Give the extent of all Plasmodium ovale-infected red blood cells.
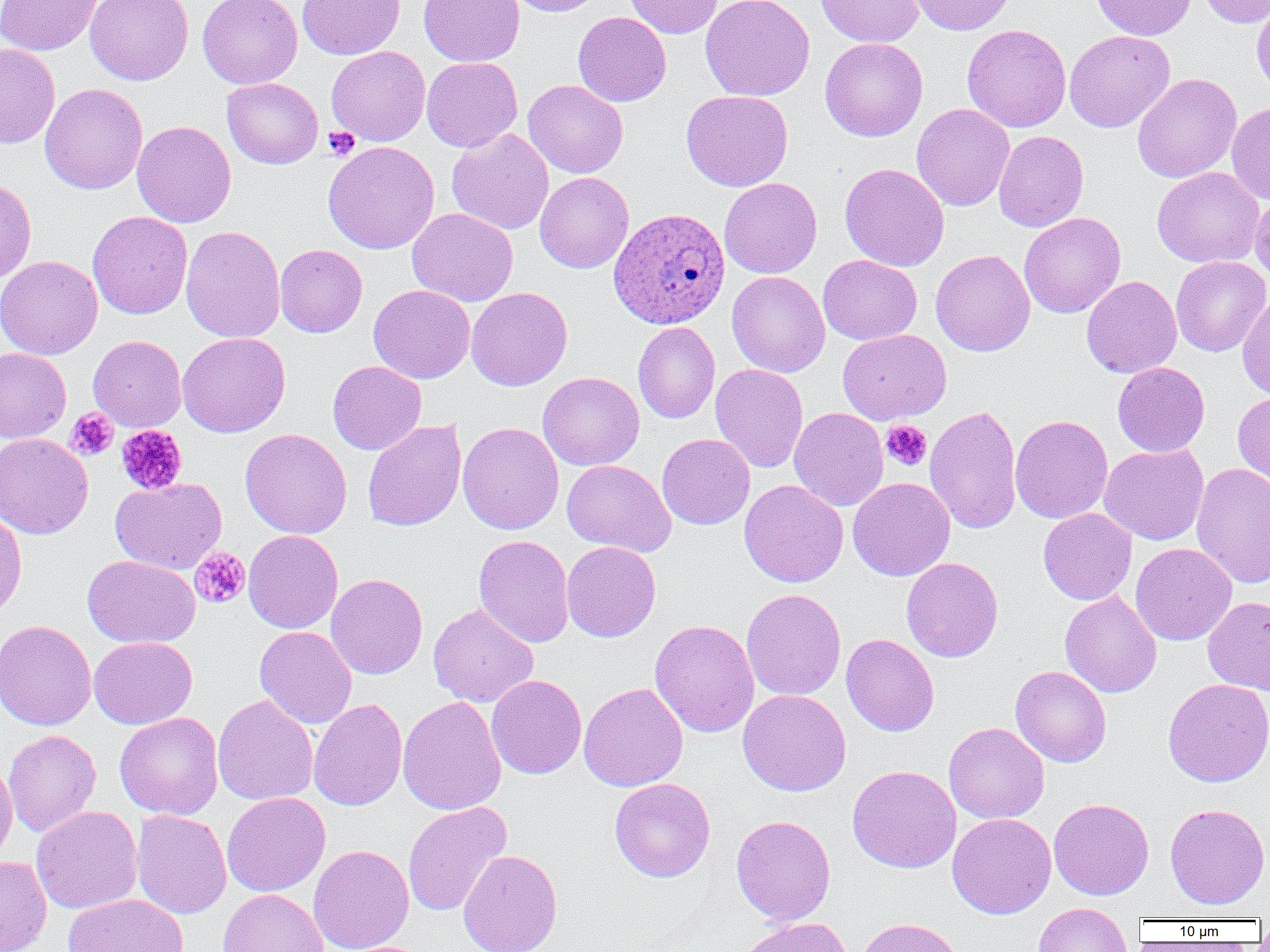

Approximate bounding boxes as (x1,y1)-(x2,y2) corner pairs in pixels.
Plasmodium ovale-infected red blood cells: (609,207)-(730,329).

{
  "slide_level_diagnosis": "Plasmodium ovale",
  "image_size": "1270×952 pixels",
  "magnification": "1000x",
  "preparation": "thin blood smear",
  "field_of_view": "one of a larger specimen",
  "modality": "light microscopy",
  "platelet_locations": "approximate bounding boxes as (x1,y1)-(x2,y2) corner pairs in pixels: (322,126)-(360,160), (64,407)-(119,461), (881,420)-(932,471), (116,424)-(188,495), (189,547)-(251,609)",
  "uninfected_red_blood_cell_locations": "approximate bounding boxes as (x1,y1)-(x2,y2) corner pairs in pixels: (0,0)-(102,55), (85,0)-(194,86), (197,0)-(303,89), (297,0)-(404,60), (419,0)-(524,67), (505,0)-(608,16), (623,0)-(723,38), (700,0)-(815,101), (815,0)-(924,47), (907,0)-(1015,35), (1091,0)-(1196,41), (1197,0)-(1270,28), (1251,2)-(1270,97), (573,11)-(672,107), (962,24)-(1071,132), (1064,30)-(1175,133), (820,37)-(928,141), (0,43)-(60,149), (326,46)-(430,146), (421,57)-(522,152), (1132,73)-(1242,183), (222,78)-(323,169), (522,79)-(628,178), (40,83)-(147,194), (681,90)-(793,191), (1227,101)-(1270,204), (911,104)-(1014,211), (132,120)-(236,228), (447,128)-(554,235), (993,130)-(1089,232), (322,141)-(439,254), (839,162)-(950,271), (1152,167)-(1264,268), (535,172)-(634,273), (0,176)-(37,283), (719,177)-(822,278), (1249,193)-(1270,283), (407,208)-(518,307), (87,211)-(192,319), (1019,212)-(1126,318), (181,225)-(285,343), (275,244)-(367,337), (930,249)-(1035,356), (818,254)-(922,345), (0,255)-(102,359), (1170,256)-(1269,356), (727,271)-(830,377), (1081,275)-(1182,378), (369,284)-(475,383), (466,287)-(572,391), (1237,292)-(1270,402), (633,322)-(720,424), (837,329)-(951,424), (178,332)-(290,437), (88,335)-(186,432), (0,347)-(71,443), (327,360)-(426,455), (1113,362)-(1210,457), (710,363)-(808,473), (537,372)-(644,471), (1233,390)-(1270,491), (924,405)-(1023,534), (789,407)-(888,511), (1010,414)-(1113,524), (362,420)-(466,532), (457,422)-(564,534), (240,428)-(352,539), (0,433)-(92,539), (657,433)-(755,530), (1099,443)-(1209,545), (562,459)-(676,556), (1191,463)-(1270,589), (847,477)-(955,581), (110,478)-(227,574), (739,479)-(848,587), (0,507)-(27,621), (1038,508)-(1137,605), (243,529)-(343,633), (473,534)-(574,648), (562,541)-(661,642), (1131,543)-(1237,646), (83,555)-(200,648), (901,557)-(1003,662), (325,573)-(427,680), (741,588)-(846,701), (1059,591)-(1162,698), (1203,596)-(1270,695), (428,603)-(538,708), (0,619)-(96,731), (650,619)-(759,737), (254,626)-(357,728), (841,634)-(939,736), (89,636)-(197,728), (1011,665)-(1111,767), (486,675)-(587,779), (1163,678)-(1270,787), (579,682)-(688,792), (738,689)-(851,796), (212,694)-(318,806), (398,696)-(506,815), (308,699)-(408,811), (115,712)-(224,820), (943,722)-(1049,824), (3,729)-(101,837), (0,759)-(17,863), (847,764)-(961,873), (609,778)-(715,882), (221,792)-(331,896), (1049,798)-(1154,900), (402,801)-(512,917), (1164,803)-(1270,910), (31,805)-(143,914), (132,810)-(232,919), (947,813)-(1056,919), (731,815)-(836,926), (307,845)-(414,952), (457,849)-(563,952), (0,855)-(52,952), (217,889)-(329,952), (62,893)-(188,952), (1033,902)-(1134,952), (736,917)-(855,952), (855,917)-(966,952)"
}